Point out each Plasmodium parasite and each leukocyte.
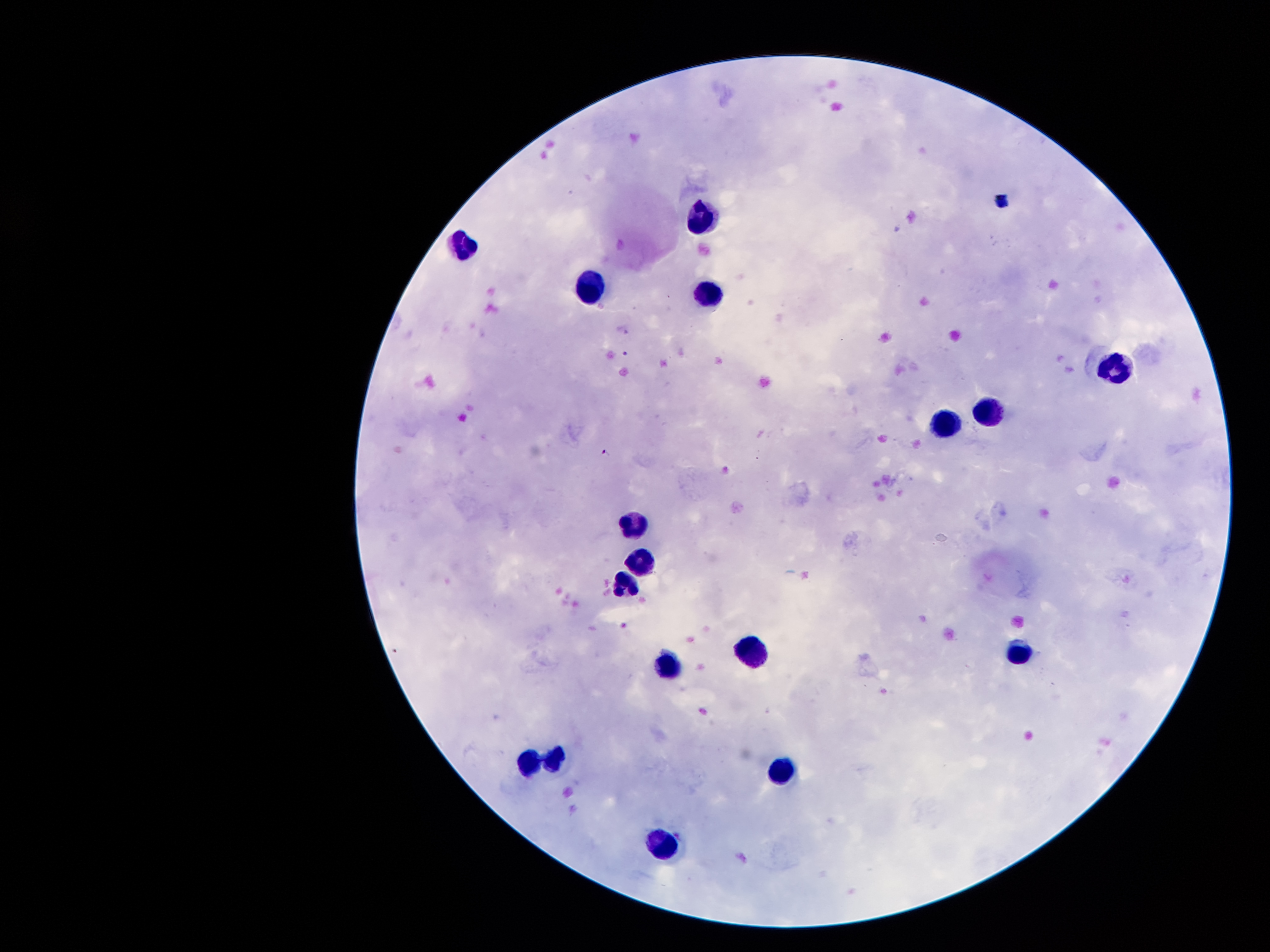

Approximate centers as (x, y) in pixels.
Plasmodium parasites: (626, 354), (607, 452).
Leukocytes: (701, 218), (461, 246), (590, 290), (711, 293), (1113, 367), (989, 413), (944, 425), (634, 525), (645, 561), (626, 583), (752, 653), (1018, 653), (670, 667), (555, 758), (525, 760), (779, 772), (668, 847).

Summary:
  - Preparation: thick peripheral-blood smear
  - Stain: Giemsa
  - Capture: smartphone through the microscope eyepiece
  - Patient malaria status: positive for Plasmodium falciparum
  - Magnification: 100x
  - Image size: 1270×952 pixels
  - Field of view: one from this slide